Classify this cell by malaria status.
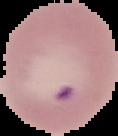

It is parasitized.

image type = segmented cell region on a black background
image size = 118×136 pixels
preparation = thin blood film